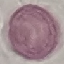 Malaria status: uninfected. Thin blood smear. Giemsa stain. Cell patch, automatically extracted from a larger field of view and resized to 64 × 64 pixels. Acquired by smartphone through the microscope eyepiece.